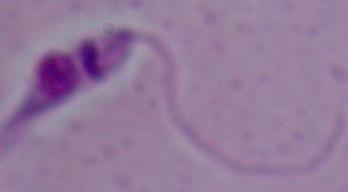

Summary:
  - Modality: photomicrograph
  - Identification: Leishmania
  - Magnification: 1000x